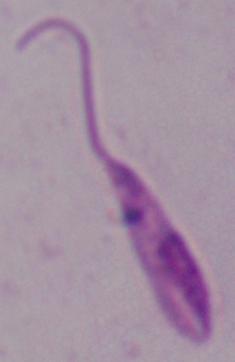

Summary:
  - Modality: micrograph
  - Magnification: 1000x
  - Identification: Leishmania